Locate every blood parasite and identify its species.
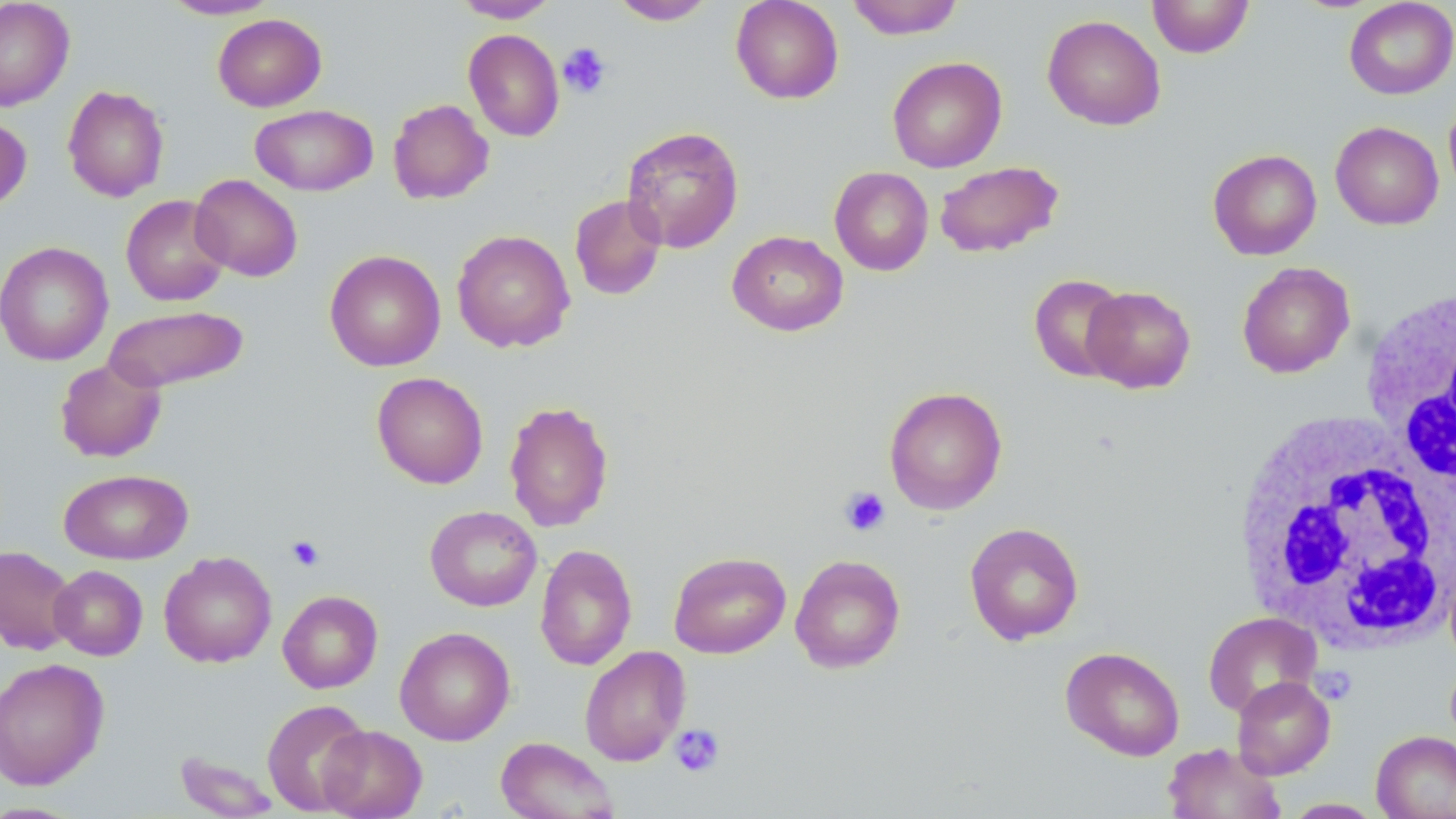
No blood parasites seen.

Approximate bounding boxes as named x1/y1/x2/y2 corners in pixels. White blood cell locations: (x1=1359, y1=286, x2=1455, y2=498), (x1=1232, y1=416, x2=1455, y2=652). Uninfected red blood cell locations: (x1=0, y1=0, x2=75, y2=111), (x1=159, y1=0, x2=281, y2=20), (x1=452, y1=0, x2=560, y2=22), (x1=609, y1=0, x2=717, y2=25), (x1=730, y1=0, x2=844, y2=104), (x1=845, y1=0, x2=965, y2=40), (x1=1147, y1=0, x2=1255, y2=58), (x1=1343, y1=0, x2=1456, y2=100), (x1=212, y1=14, x2=327, y2=112), (x1=1042, y1=14, x2=1166, y2=131), (x1=463, y1=29, x2=564, y2=141), (x1=887, y1=56, x2=1007, y2=173), (x1=62, y1=85, x2=169, y2=202), (x1=1444, y1=94, x2=1456, y2=202), (x1=388, y1=98, x2=494, y2=204), (x1=250, y1=104, x2=378, y2=196), (x1=0, y1=115, x2=32, y2=212), (x1=1330, y1=121, x2=1444, y2=230), (x1=621, y1=126, x2=744, y2=253), (x1=1208, y1=149, x2=1322, y2=260), (x1=934, y1=160, x2=1064, y2=258), (x1=829, y1=166, x2=933, y2=276), (x1=190, y1=174, x2=302, y2=282), (x1=121, y1=194, x2=232, y2=306), (x1=568, y1=194, x2=667, y2=301), (x1=452, y1=229, x2=575, y2=353), (x1=727, y1=230, x2=848, y2=337), (x1=0, y1=241, x2=114, y2=366), (x1=324, y1=250, x2=446, y2=371), (x1=1237, y1=261, x2=1355, y2=378), (x1=1029, y1=274, x2=1130, y2=382), (x1=1082, y1=285, x2=1196, y2=393), (x1=104, y1=305, x2=248, y2=393), (x1=54, y1=358, x2=167, y2=463), (x1=372, y1=371, x2=488, y2=489), (x1=884, y1=386, x2=1007, y2=515), (x1=503, y1=400, x2=614, y2=532), (x1=58, y1=468, x2=193, y2=565), (x1=425, y1=505, x2=542, y2=611), (x1=965, y1=521, x2=1084, y2=645), (x1=534, y1=543, x2=637, y2=671), (x1=0, y1=545, x2=79, y2=656), (x1=159, y1=551, x2=276, y2=668), (x1=669, y1=551, x2=791, y2=659), (x1=790, y1=554, x2=906, y2=673), (x1=49, y1=565, x2=148, y2=660), (x1=277, y1=590, x2=383, y2=693), (x1=1203, y1=612, x2=1322, y2=718), (x1=395, y1=626, x2=515, y2=745), (x1=579, y1=645, x2=691, y2=766), (x1=1061, y1=646, x2=1185, y2=761), (x1=0, y1=657, x2=110, y2=790), (x1=1232, y1=676, x2=1336, y2=779), (x1=262, y1=699, x2=372, y2=815), (x1=318, y1=725, x2=427, y2=818), (x1=1371, y1=730, x2=1456, y2=819), (x1=494, y1=736, x2=619, y2=819), (x1=1163, y1=742, x2=1287, y2=819), (x1=174, y1=751, x2=280, y2=819), (x1=1281, y1=798, x2=1385, y2=818). Platelet locations: (x1=558, y1=42, x2=612, y2=98), (x1=840, y1=486, x2=890, y2=536), (x1=286, y1=535, x2=324, y2=571), (x1=670, y1=724, x2=725, y2=777). Slide-level diagnosis: no evidence of blood parasites. Thin blood film. May-Grünwald-Giemsa stain. Single field of view. Image is 1456×819 pixels. Light microscopy. 1000x magnification.